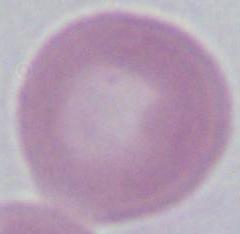

Summary:
  - Identification: erythrocyte
  - Magnification: 1000x
  - Modality: photomicrograph